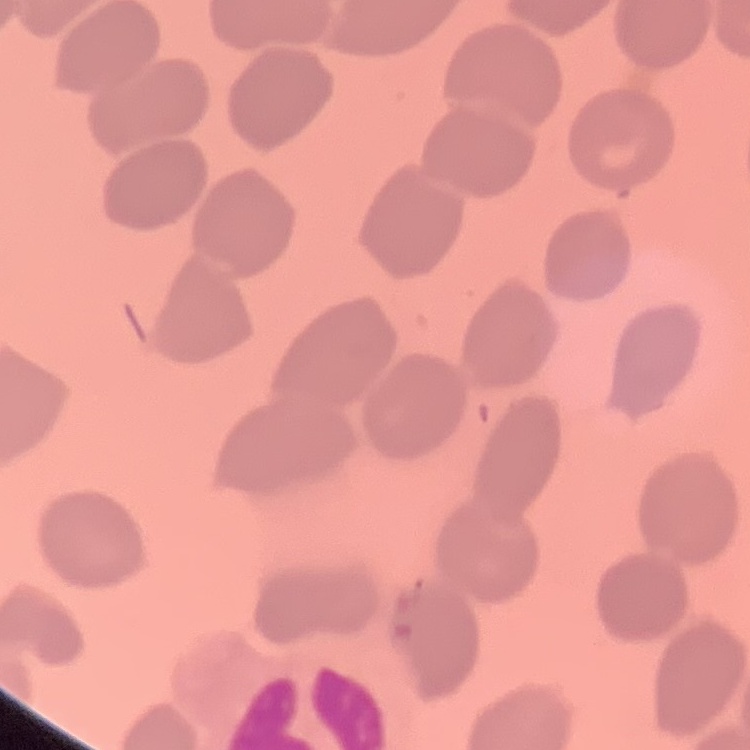
Summary:
  - Erythrocyte morphology: no rouleaux formation
  - Preparation: thin peripheral smear
  - Image type: square crop of a larger photomicrograph
  - Stain: Field's or Giemsa